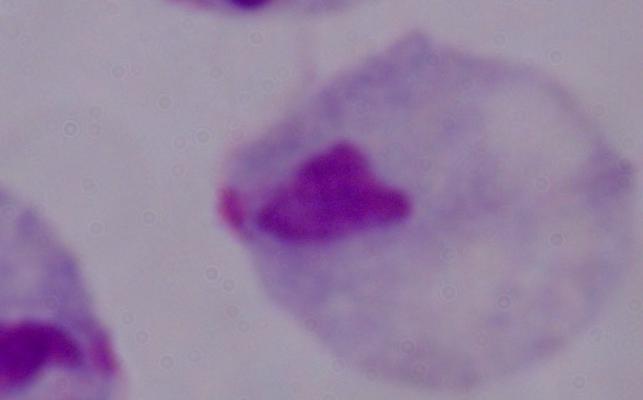
identification: trichomonad
magnification: 1000x
modality: micrograph